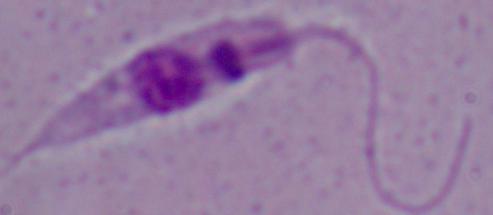

Summary:
  - Identification: Leishmania
  - Modality: micrograph
  - Magnification: 1000x